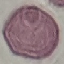
malaria_status: uninfected
image_type: cell patch, automatically extracted from a larger field of view and resized to 64 × 64 pixels
stain: Giemsa
capture: smartphone through the microscope eyepiece
preparation: thin smear